Report the malaria status of this cell.
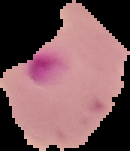

Parasitized.

image_size: 130×151 pixels
image_type: segmented cell region with the area outside set to black
preparation: thin blood film